Classify this cell by malaria status.
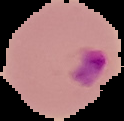
Parasitized.

image type = segmented cell region on a black background
image size = 124×121 pixels
preparation = thin blood film